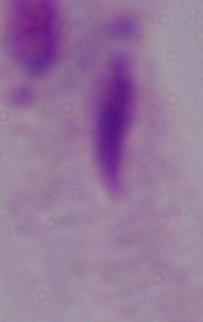

Micrograph. Captured at 1000x magnification. A trichomonad is shown.